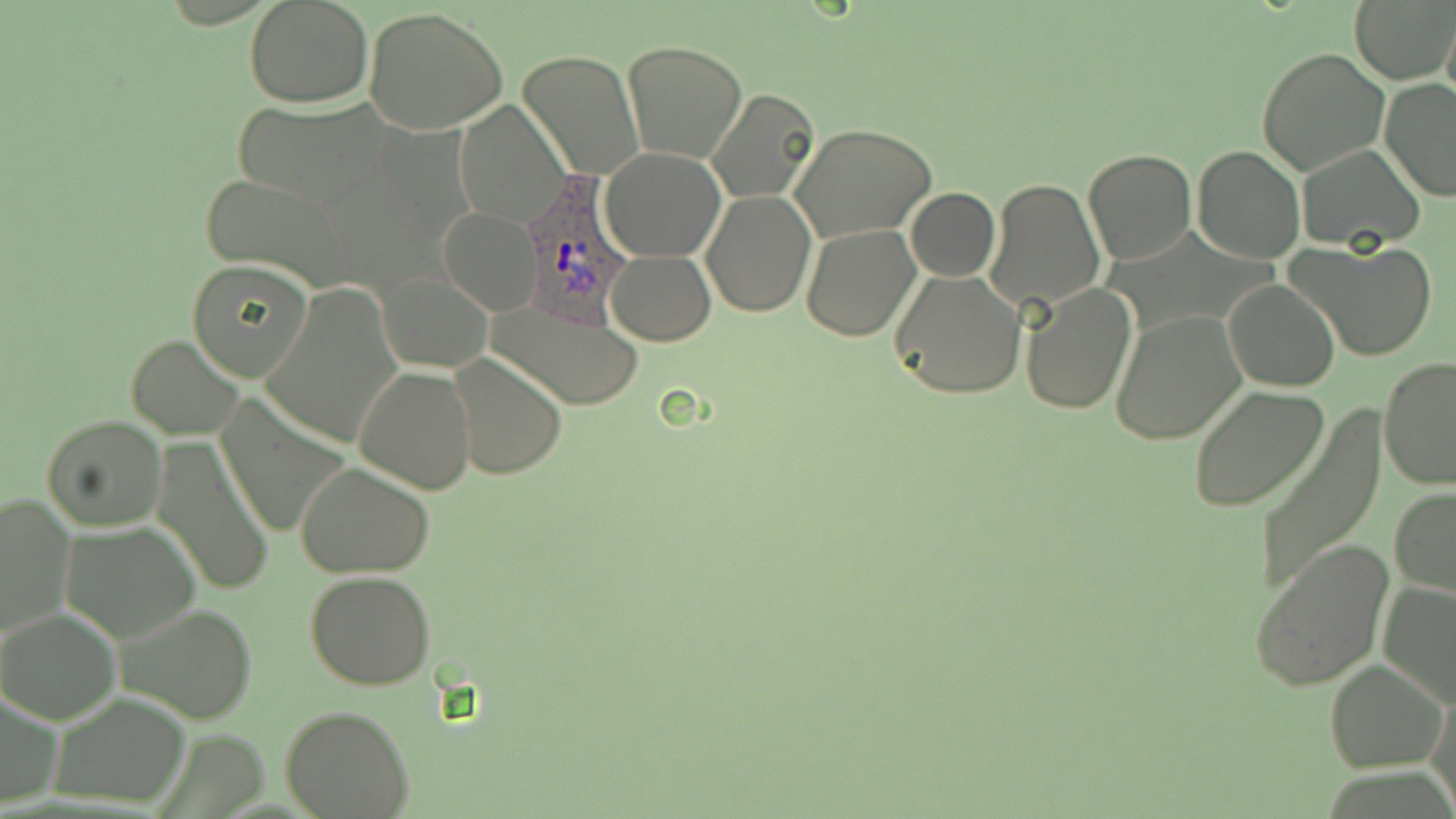
Summary:
  - Coordinate format: approximate bounding boxes as [x1, y1, x2, y2] in pixels
  - Plasmodium ovale-infected red blood cell locations: [520, 183, 633, 323]
  - Uninfected red blood cell locations: [245, 0, 373, 107], [1350, 0, 1456, 85], [365, 7, 511, 136], [1442, 12, 1456, 110], [622, 40, 747, 164], [1258, 47, 1389, 177], [518, 51, 643, 180], [1379, 79, 1456, 202], [704, 87, 822, 205], [232, 100, 390, 207], [455, 100, 570, 229], [791, 123, 936, 243], [1295, 143, 1426, 251], [1192, 144, 1304, 263], [601, 147, 725, 261], [1082, 147, 1197, 265], [197, 174, 355, 287], [984, 177, 1106, 313], [905, 187, 999, 283], [702, 191, 815, 317], [438, 209, 541, 315], [800, 225, 920, 341], [1288, 238, 1437, 363], [606, 250, 716, 345], [186, 260, 313, 382], [887, 267, 1027, 400], [378, 272, 493, 372], [1224, 278, 1340, 392], [263, 281, 404, 450], [1021, 284, 1137, 414], [489, 297, 643, 410], [1110, 311, 1246, 444], [126, 334, 245, 439], [447, 352, 567, 480], [1378, 356, 1456, 488], [354, 364, 477, 495], [1187, 386, 1330, 512], [215, 397, 349, 542], [1252, 410, 1389, 595], [40, 416, 167, 532], [151, 438, 276, 598], [294, 461, 436, 577], [1390, 487, 1456, 597], [1, 491, 74, 640], [61, 522, 202, 644], [1247, 539, 1395, 692], [305, 571, 437, 692], [1378, 579, 1456, 709], [115, 603, 258, 726], [1, 609, 121, 724], [1324, 658, 1449, 771], [1427, 683, 1456, 813], [1, 689, 64, 811], [49, 692, 191, 807], [284, 706, 414, 818]
  - Slide-level diagnosis: Plasmodium ovale
  - Image size: 1456×819 pixels
  - Preparation: thin blood smear
  - Stain: May-Grünwald-Giemsa
  - Modality: light microscopy
  - Field of view: one of a larger specimen
  - Magnification: 1000x